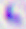

Photomicrograph. Captured at 400x magnification. Toxoplasma gondii is seen.